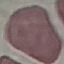

Summary:
  - Malaria status: uninfected
  - Capture: smartphone through the microscope eyepiece
  - Stain: Giemsa
  - Image type: automatically extracted cell patch, resized to 64 × 64 pixels
  - Preparation: thin smear